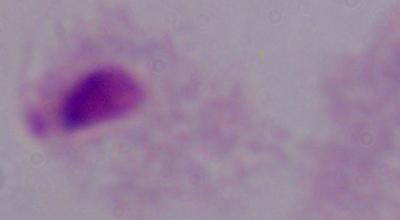
Summary:
  - Identification: trichomonad
  - Modality: photomicrograph
  - Magnification: 1000x